Comment on the morphology of the red blood cells.
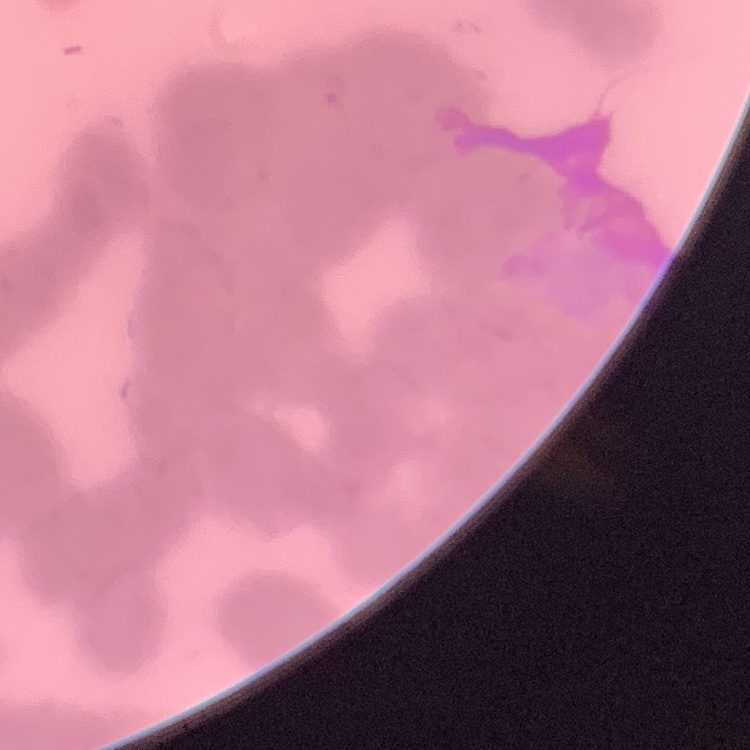

They show rouleaux formation.

Summary:
  - Preparation: thin peripheral smear
  - Stain: Field's or Giemsa
  - Image type: one tile cut from a larger photomicrograph